Point out each Plasmodium parasite and each leukocyte.
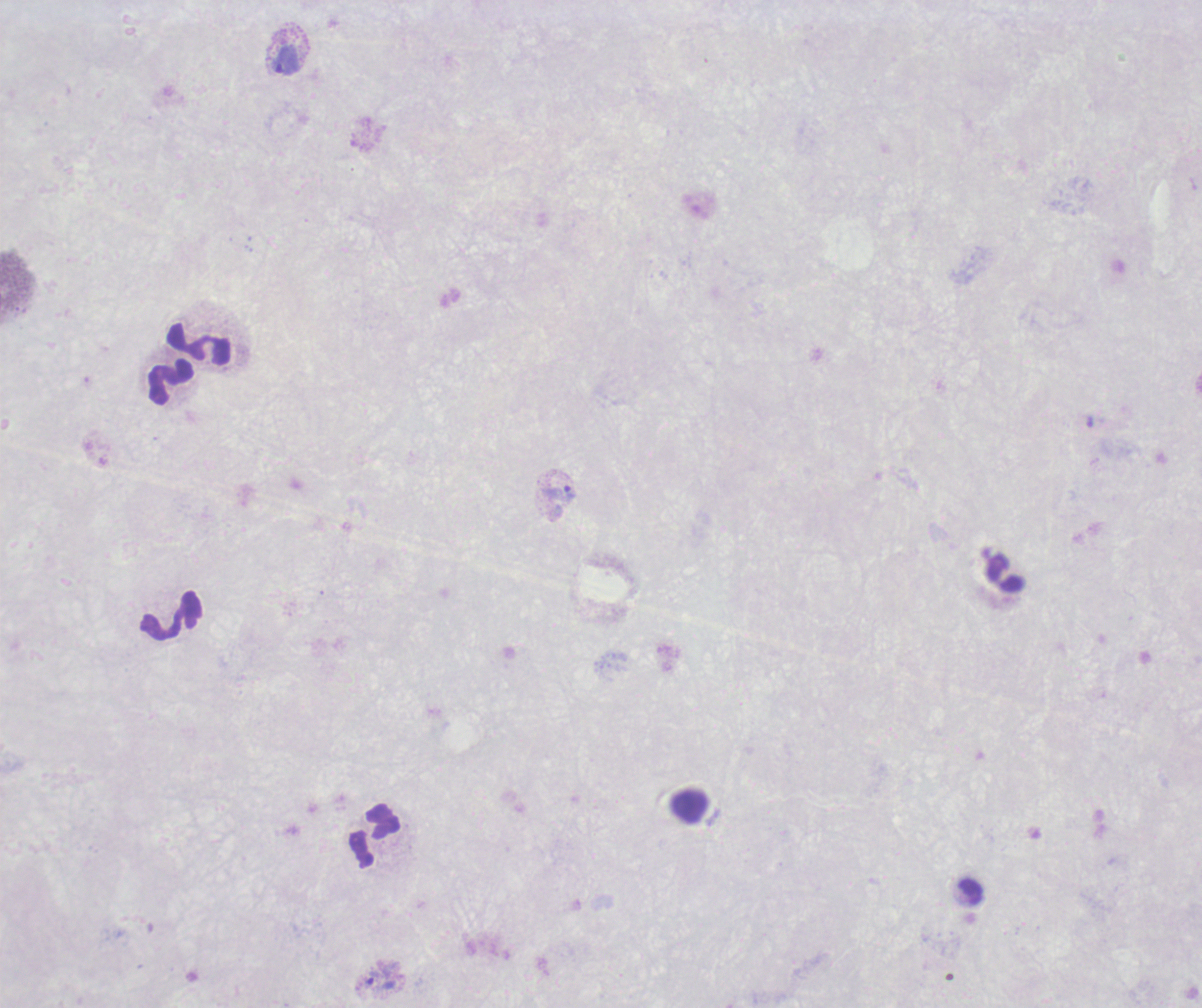

Approximate centers as (x, y) in pixels.
Trophozoites: (286, 60), (559, 493), (372, 978).
No schizont or gametocyte forms observed.
Leukocytes: (199, 344), (171, 381), (1005, 573), (171, 615), (690, 805), (375, 836).

Summary:
  - Magnification: 100x
  - Preparation: thick blood film
  - Background quality: unsatisfactory
  - Image size: 1202×1008 pixels
  - Field of view: single
  - Coloration quality: bad
  - Context: previously used in an actual diagnosis
  - Stain: Romanowsky